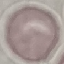

Summary:
  - Malaria status: uninfected
  - Stain: Giemsa
  - Capture: smartphone camera at the microscope eyepiece
  - Preparation: thin smear
  - Image type: automatically extracted cell patch, resized to 64 × 64 pixels